Classify this cell by malaria status.
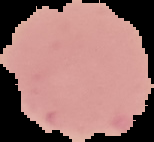

Uninfected.

From a thin blood film. Image is 154×142 pixels. Segmented cell region on a black background.